Classify this cell by malaria status.
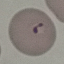
Parasitized.

image_type: automatically extracted cell patch, resized to 64 × 64 pixels
capture: smartphone through the microscope eyepiece
preparation: thin blood smear
stain: Giemsa